Locate every uninfected red blood cell.
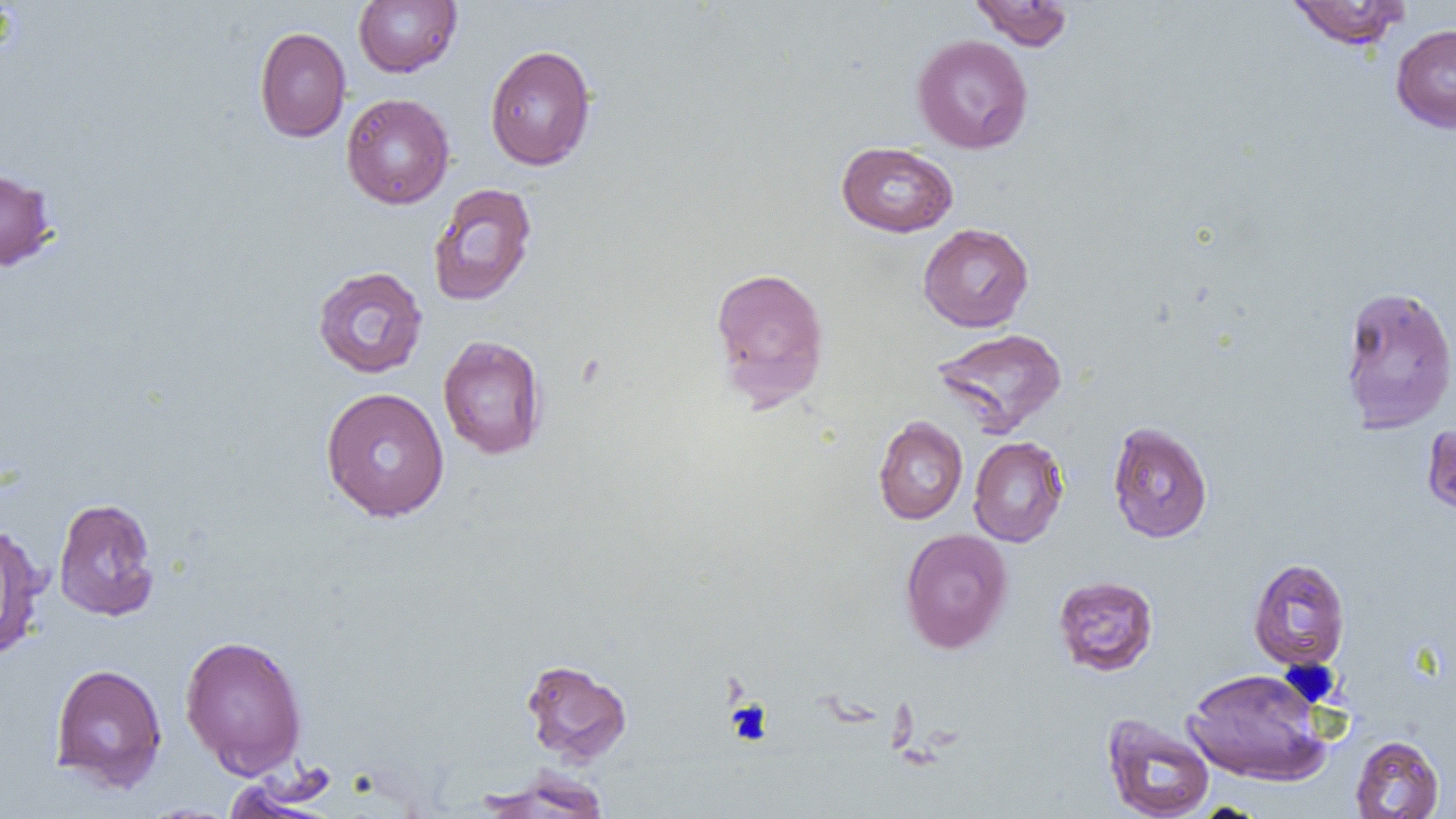
Approximate bounding boxes as (x1, y1, x2, y2) in pixels.
Uninfected red blood cells: (353, 0, 461, 77), (968, 0, 1075, 50), (1285, 0, 1411, 50), (1390, 24, 1456, 133), (254, 26, 351, 142), (912, 34, 1033, 154), (484, 44, 597, 171), (341, 93, 455, 209), (836, 141, 958, 237), (0, 167, 58, 272), (427, 183, 538, 307), (918, 223, 1034, 332), (709, 265, 830, 410), (312, 266, 428, 378), (1337, 284, 1455, 434), (930, 327, 1067, 437), (438, 334, 548, 460), (320, 387, 450, 522), (873, 416, 968, 525), (1107, 421, 1213, 543), (1421, 422, 1456, 519), (968, 436, 1068, 547), (52, 496, 160, 621), (0, 521, 47, 661), (899, 528, 1013, 654), (1247, 557, 1351, 670), (1052, 575, 1159, 677), (179, 633, 308, 778), (521, 658, 632, 765), (49, 662, 168, 793), (1182, 667, 1332, 786), (1102, 713, 1215, 819), (1350, 735, 1444, 818), (476, 768, 612, 818).

slide_level_diagnosis: no evidence of blood parasites
platelet_locations: 'approximate bounding boxes as (x1, y1, x2, y2) in pixels: (726, 700, 772, 744)'
preparation: thin blood smear
field_of_view: one of a larger specimen
magnification: 1000x
image_size: 1456×819 pixels
modality: optical microscopy